Name the parasite shown.
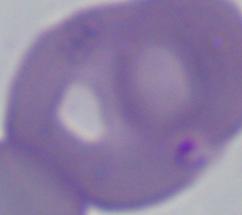

This is Babesia.

magnification = 1000x
modality = photomicrograph